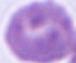
Summary:
  - Magnification: 1000x
  - Identification: erythrocyte
  - Modality: photomicrograph